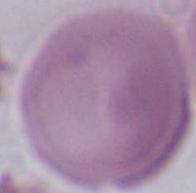

Summary:
  - Identification: red blood cell
  - Magnification: 1000x
  - Modality: photomicrograph